Identify the parasite.
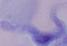

A trypanosome.

modality = photomicrograph
magnification = 1000x